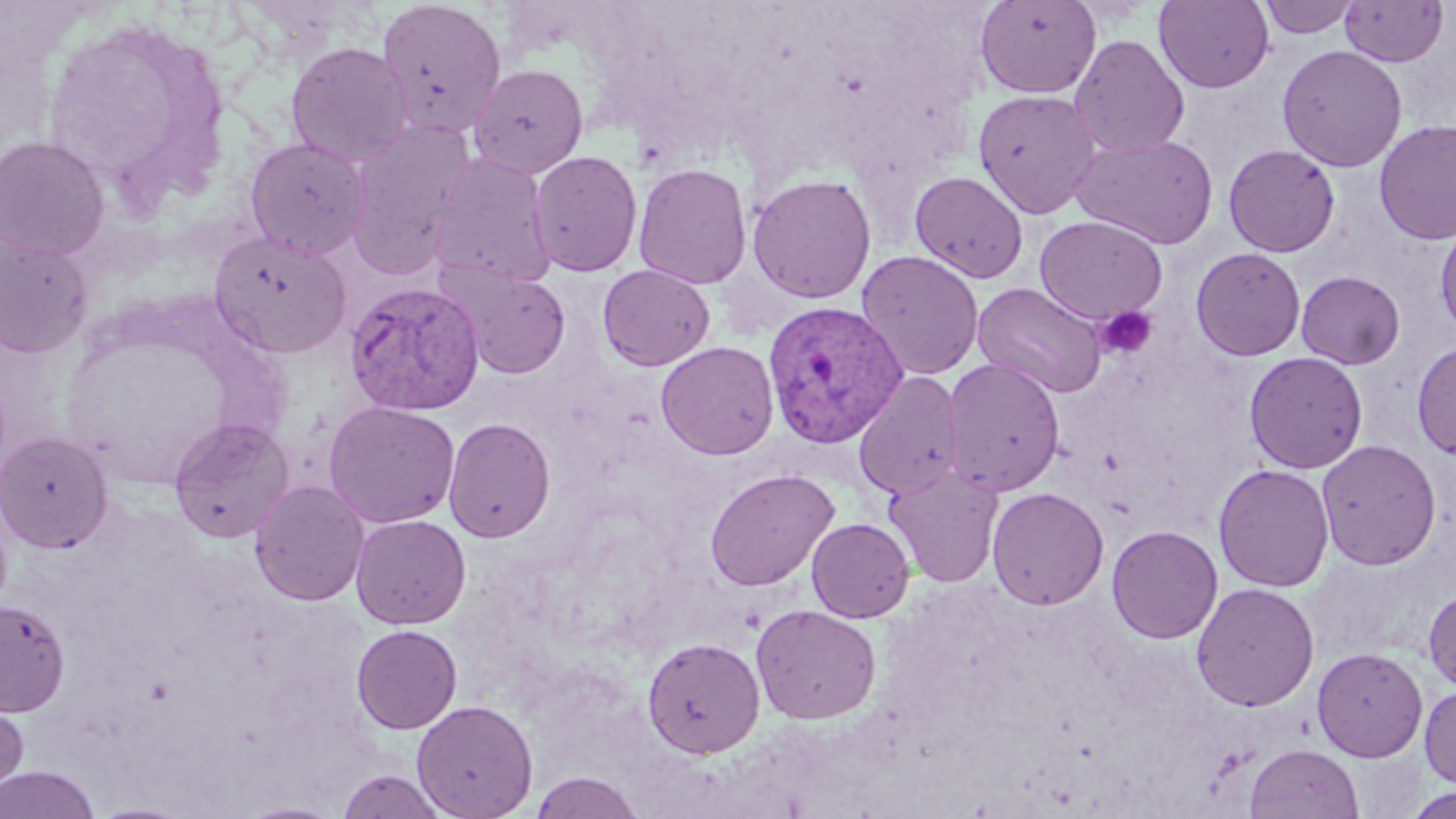

Summary:
  - Coordinate format: approximate bounding boxes as named x1/y1/x2/y2 corners in pixels
  - Uninfected red blood cell locations: (x1=375, y1=0, x2=507, y2=138), (x1=975, y1=0, x2=1101, y2=99), (x1=1154, y1=0, x2=1274, y2=93), (x1=1257, y1=0, x2=1361, y2=39), (x1=1340, y1=0, x2=1449, y2=67), (x1=44, y1=23, x2=228, y2=196), (x1=1069, y1=34, x2=1190, y2=158), (x1=285, y1=42, x2=413, y2=166), (x1=1277, y1=44, x2=1407, y2=172), (x1=469, y1=63, x2=589, y2=178), (x1=973, y1=88, x2=1103, y2=218), (x1=1374, y1=119, x2=1456, y2=246), (x1=345, y1=121, x2=477, y2=278), (x1=1070, y1=132, x2=1219, y2=249), (x1=0, y1=135, x2=110, y2=261), (x1=244, y1=136, x2=370, y2=259), (x1=927, y1=143, x2=1086, y2=269), (x1=1223, y1=144, x2=1340, y2=257), (x1=528, y1=150, x2=643, y2=277), (x1=427, y1=152, x2=557, y2=291), (x1=632, y1=162, x2=753, y2=290), (x1=910, y1=170, x2=1029, y2=283), (x1=747, y1=173, x2=877, y2=304), (x1=1035, y1=215, x2=1168, y2=324), (x1=1434, y1=219, x2=1456, y2=339), (x1=209, y1=231, x2=351, y2=359), (x1=0, y1=233, x2=94, y2=358), (x1=1191, y1=247, x2=1306, y2=361), (x1=857, y1=250, x2=984, y2=381), (x1=598, y1=264, x2=715, y2=370), (x1=443, y1=265, x2=572, y2=379), (x1=1296, y1=270, x2=1406, y2=369), (x1=972, y1=282, x2=1108, y2=398), (x1=655, y1=341, x2=779, y2=460), (x1=1412, y1=341, x2=1456, y2=460), (x1=1244, y1=351, x2=1368, y2=474), (x1=942, y1=358, x2=1066, y2=496), (x1=853, y1=371, x2=965, y2=499), (x1=323, y1=401, x2=461, y2=528), (x1=167, y1=417, x2=295, y2=545), (x1=443, y1=417, x2=556, y2=543), (x1=0, y1=430, x2=113, y2=552), (x1=1316, y1=439, x2=1441, y2=570), (x1=1213, y1=463, x2=1335, y2=592), (x1=884, y1=464, x2=1005, y2=588), (x1=704, y1=468, x2=840, y2=591), (x1=249, y1=480, x2=369, y2=606), (x1=987, y1=486, x2=1109, y2=610), (x1=351, y1=514, x2=471, y2=630), (x1=806, y1=517, x2=915, y2=622), (x1=1106, y1=525, x2=1223, y2=644), (x1=1190, y1=582, x2=1320, y2=711), (x1=1423, y1=586, x2=1456, y2=693), (x1=0, y1=598, x2=70, y2=715), (x1=750, y1=603, x2=882, y2=724), (x1=351, y1=624, x2=462, y2=734), (x1=642, y1=636, x2=765, y2=758), (x1=1312, y1=646, x2=1428, y2=762), (x1=1419, y1=683, x2=1456, y2=789), (x1=0, y1=691, x2=30, y2=804), (x1=411, y1=699, x2=539, y2=818), (x1=1246, y1=743, x2=1364, y2=819), (x1=0, y1=765, x2=101, y2=818), (x1=335, y1=768, x2=449, y2=818), (x1=529, y1=771, x2=646, y2=819), (x1=1403, y1=785, x2=1456, y2=818), (x1=237, y1=799, x2=348, y2=819), (x1=86, y1=800, x2=203, y2=818)
  - Platelet locations: (x1=1096, y1=306, x2=1158, y2=359)
  - Plasmodium vivax-infected red blood cell locations: (x1=344, y1=281, x2=485, y2=417), (x1=762, y1=298, x2=909, y2=449)
  - Slide-level diagnosis: Plasmodium vivax
  - Image size: 1456×819 pixels
  - Magnification: 1000x
  - Stain: May-Grünwald-Giemsa
  - Modality: light microscopy
  - Preparation: thin blood smear
  - Field of view: single